Classify this cell by malaria status.
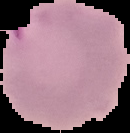

It is parasitized.

Segmented cell region on a black background. From a thin blood smear. Image is 130×133 pixels.